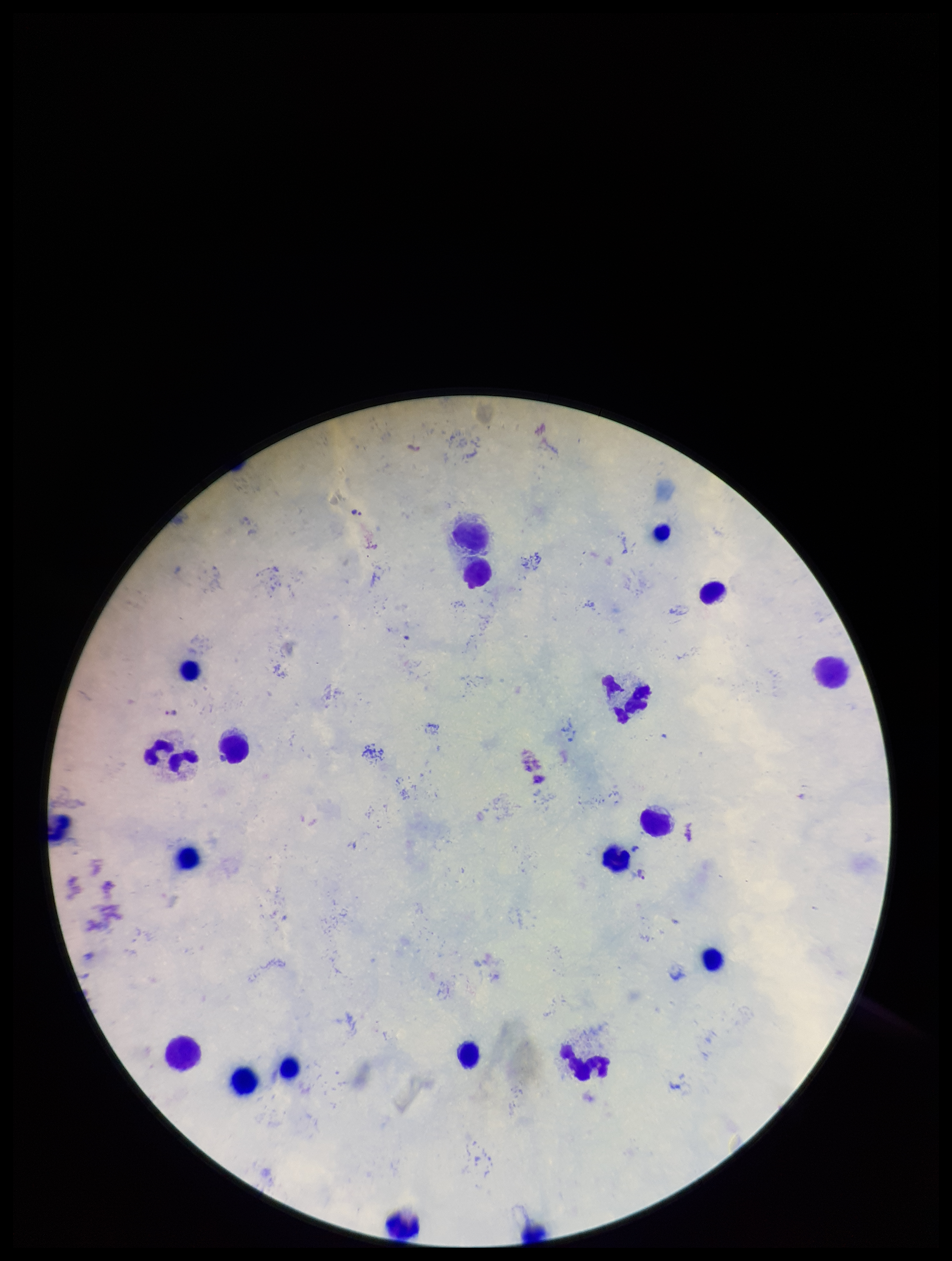

Summary:
  - Field of view: single
  - Plasmodium parasites: seen
  - Leukocyte count: 22
  - Patient malaria status: infected
  - Capture: smartphone photograph through the microscope eyepiece
  - Species reported for this patient: Plasmodium falciparum
  - Image size: 952×1261 pixels
  - Parasite count: 3
  - Preparation: thick blood smear
  - Stain: Giemsa